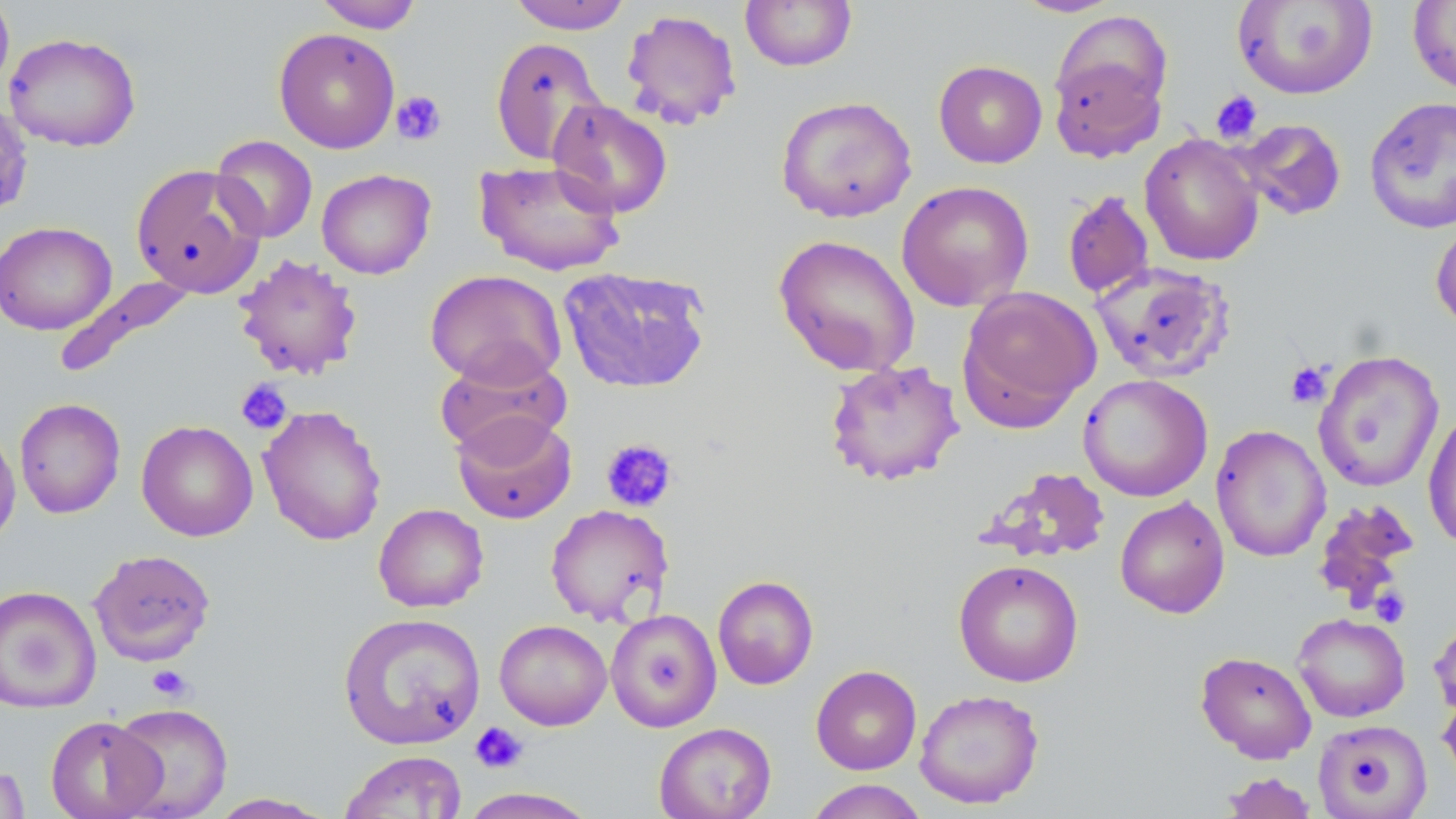
Approximate bounding boxes as (x1, y1, x2, y2) in pixels. Uninfected red blood cell locations: (0, 0, 15, 99), (312, 0, 423, 32), (507, 0, 634, 34), (1009, 0, 1125, 18), (1232, 0, 1378, 100), (1407, 0, 1456, 97), (740, 1, 857, 72), (620, 8, 743, 131), (1048, 27, 1170, 161), (273, 28, 400, 153), (3, 32, 142, 152), (490, 36, 608, 165), (933, 60, 1047, 168), (776, 95, 917, 223), (1364, 96, 1456, 234), (548, 99, 673, 217), (1233, 118, 1348, 221), (1139, 133, 1264, 267), (210, 135, 318, 243), (475, 159, 626, 276), (131, 163, 267, 299), (316, 168, 436, 279), (896, 180, 1034, 312), (1061, 189, 1155, 299), (1430, 217, 1456, 332), (0, 220, 116, 335), (773, 233, 921, 377), (233, 253, 364, 381), (1089, 262, 1236, 383), (558, 265, 712, 394), (425, 269, 567, 389), (53, 276, 197, 379), (957, 286, 1101, 430), (434, 350, 571, 459), (1313, 350, 1445, 493), (823, 359, 965, 487), (1078, 374, 1213, 502), (14, 397, 126, 518), (258, 405, 387, 546), (1423, 409, 1456, 551), (451, 411, 577, 524), (136, 420, 258, 542), (0, 421, 21, 550), (1210, 424, 1331, 562), (978, 466, 1113, 563), (1115, 496, 1230, 618), (1310, 498, 1420, 618), (373, 504, 489, 613), (545, 504, 674, 627), (89, 549, 216, 666), (953, 559, 1084, 687), (712, 575, 819, 690), (0, 585, 101, 714), (605, 608, 721, 732), (338, 612, 486, 751), (1292, 612, 1410, 722), (1430, 614, 1456, 720), (493, 620, 612, 730), (1195, 650, 1317, 763), (811, 665, 922, 775), (914, 688, 1045, 809), (1438, 689, 1456, 787), (109, 702, 234, 819), (45, 715, 165, 819), (1313, 719, 1432, 819), (654, 722, 776, 819), (339, 751, 467, 818), (0, 758, 30, 819), (1220, 772, 1318, 818), (803, 779, 930, 819), (456, 787, 603, 818), (206, 793, 336, 818). Platelet locations: (390, 90, 447, 146), (1210, 90, 1263, 144), (1285, 360, 1334, 408), (235, 378, 292, 435), (600, 438, 678, 514), (1369, 587, 1410, 627), (147, 665, 194, 702), (470, 721, 528, 773). Slide-level diagnosis: no evidence of blood parasites. 1000x magnification. Single field of view. Image is 1456×819 pixels. Thin blood film. Light microscopy. May-Grünwald-Giemsa stain.